Outline each Plasmodium falciparum-infected red blood cell.
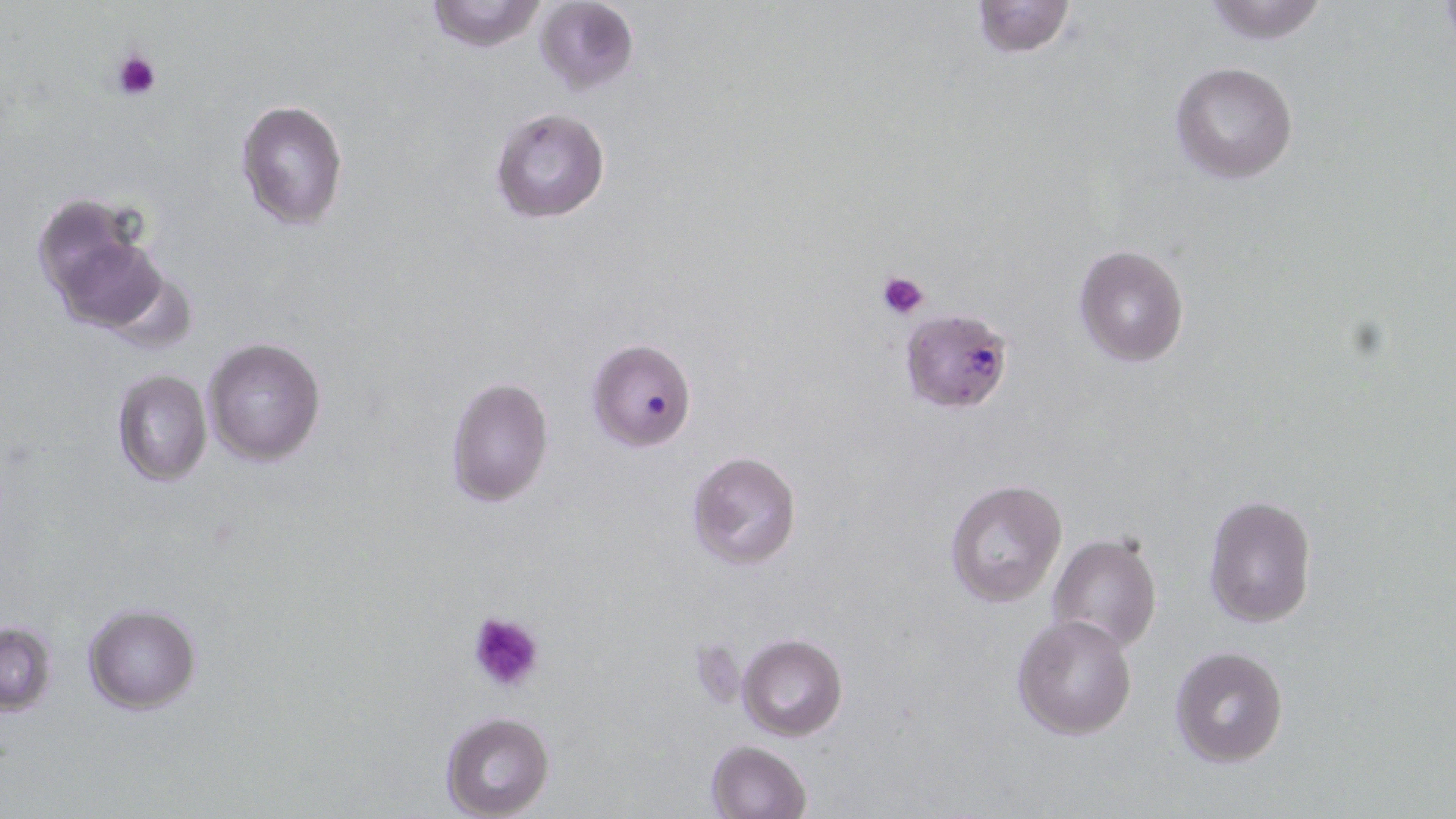
Approximate bounding boxes as named x1/y1/x2/y2 corners in pixels.
Plasmodium falciparum-infected red blood cells: (x1=905, y1=320, x2=1011, y2=412), (x1=587, y1=339, x2=696, y2=450).

slide-level diagnosis = Plasmodium falciparum
image size = 1456×819 pixels
magnification = 1000x
preparation = thin blood smear
uninfected red blood cell locations = approximate bounding boxes as named x1/y1/x2/y2 corners in pixels: (x1=423, y1=0, x2=549, y2=53), (x1=533, y1=0, x2=641, y2=97), (x1=970, y1=0, x2=1075, y2=58), (x1=1200, y1=1, x2=1333, y2=44), (x1=1170, y1=61, x2=1299, y2=184), (x1=235, y1=97, x2=350, y2=232), (x1=488, y1=107, x2=611, y2=224), (x1=32, y1=196, x2=168, y2=332), (x1=1072, y1=242, x2=1190, y2=367), (x1=202, y1=337, x2=326, y2=465), (x1=111, y1=369, x2=213, y2=487), (x1=445, y1=377, x2=551, y2=506), (x1=684, y1=452, x2=801, y2=571), (x1=944, y1=480, x2=1070, y2=608), (x1=1203, y1=493, x2=1318, y2=627), (x1=1046, y1=533, x2=1161, y2=655), (x1=82, y1=605, x2=201, y2=713), (x1=1011, y1=613, x2=1139, y2=740), (x1=0, y1=621, x2=57, y2=713), (x1=737, y1=634, x2=848, y2=741), (x1=1169, y1=645, x2=1289, y2=768), (x1=440, y1=711, x2=556, y2=819), (x1=705, y1=740, x2=812, y2=819)
modality = optical microscopy
platelet locations = approximate bounding boxes as named x1/y1/x2/y2 corners in pixels: (x1=111, y1=47, x2=164, y2=102), (x1=878, y1=269, x2=931, y2=319), (x1=466, y1=610, x2=545, y2=694)
stain = May-Grünwald-Giemsa
field of view = single